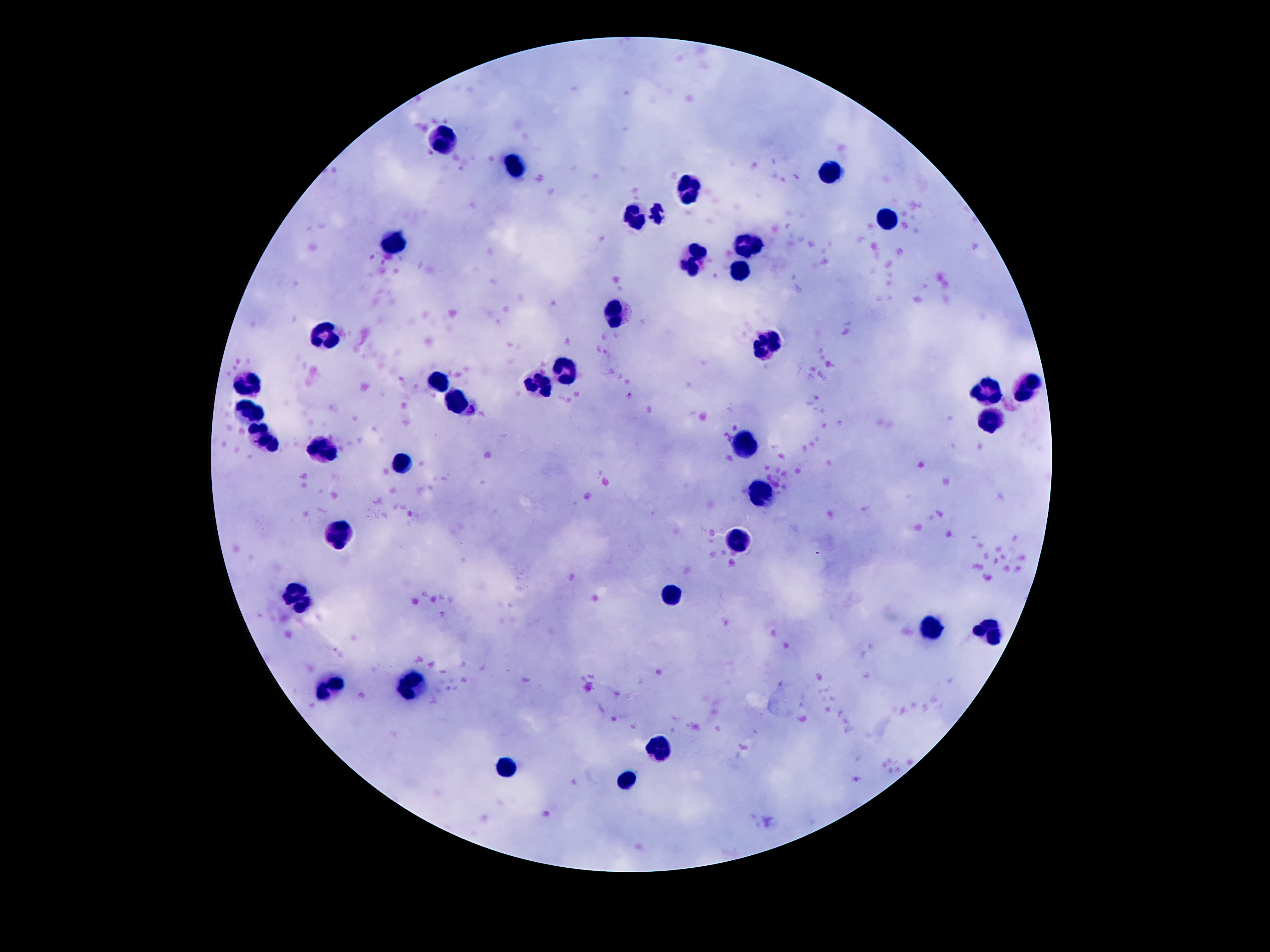
Approximate centers as [x, y] in pixels. Leukocyte locations: [446, 138], [516, 166], [832, 175], [693, 191], [657, 212], [638, 216], [883, 218], [397, 240], [748, 245], [695, 262], [737, 269], [620, 311], [327, 336], [768, 344], [438, 379], [249, 384], [1028, 388], [987, 394], [460, 404], [253, 410], [991, 421], [264, 434], [747, 440], [317, 451], [405, 464], [758, 488], [340, 539], [739, 541], [669, 593], [301, 595], [930, 629], [987, 633], [335, 682], [417, 684], [658, 746], [509, 770], [626, 780]. Image is 1270×952 pixels. Smartphone photograph taken through the microscope eyepiece. Patient malaria status: not infected. Giemsa-stained preparation. Thick blood smear. 100x magnification. Single field of view.